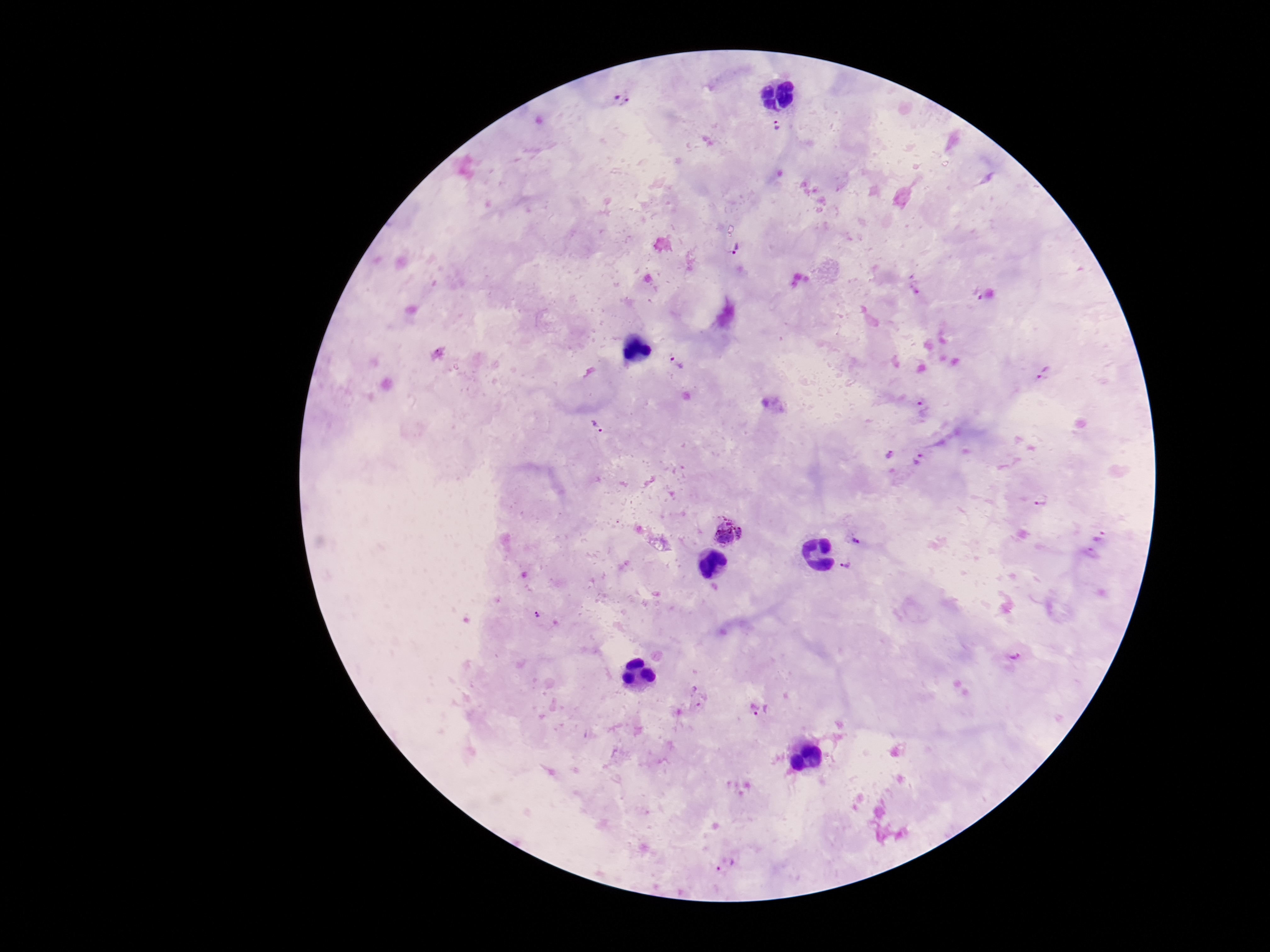
Approximate centers as [x, y] in pixels.
Summary:
  - Plasmodium parasite locations: [622, 99], [778, 126], [736, 247], [976, 294], [677, 363], [1044, 372], [924, 411], [597, 426], [889, 456], [920, 460], [1041, 499], [729, 533], [1099, 537], [856, 541], [844, 566], [1015, 654], [760, 711], [725, 865]
  - Magnification: 100x
  - Field of view: single
  - Capture: smartphone camera through the microscope eyepiece
  - Preparation: thick peripheral-blood smear
  - Patient malaria status: infected
  - Stain: Giemsa
  - Image size: 1270×952 pixels